Outline each Plasmodium ovale-infected red blood cell.
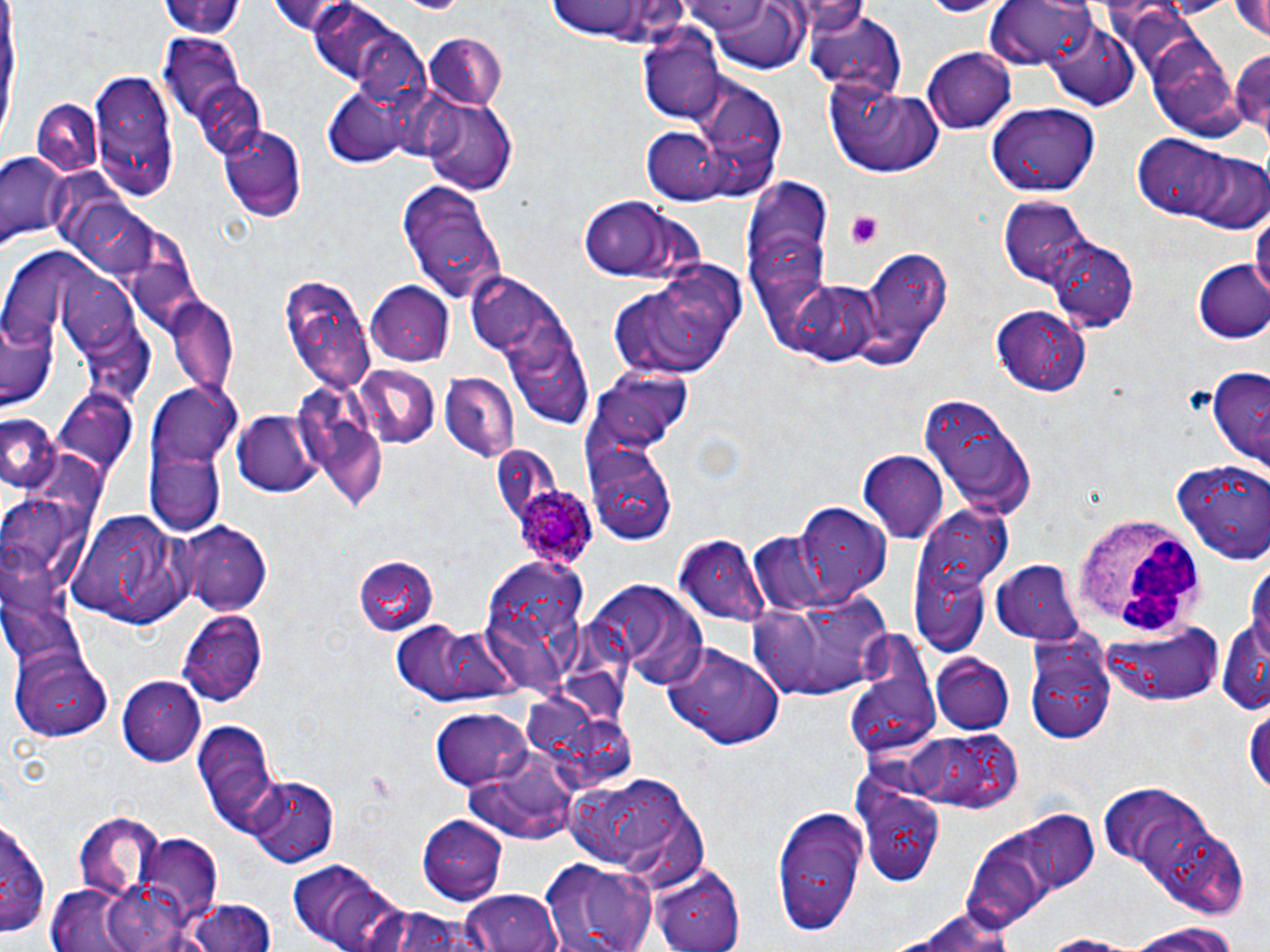

Approximate bounding boxes as (x1,y1)-(x2,y2) corner pairs in pixels.
Plasmodium ovale-infected red blood cells: (515,485)-(602,571).

White blood cell locations: (1070,515)-(1203,641). Platelet locations: (845,210)-(887,249), (364,771)-(395,799). Uninfected red blood cell locations: (154,0)-(246,42), (267,0)-(367,37), (542,0)-(693,47), (698,0)-(813,74), (985,0)-(1098,70), (1228,0)-(1270,44), (921,1)-(1000,17), (303,3)-(428,93), (800,7)-(908,98), (1046,24)-(1137,109), (638,29)-(726,124), (425,33)-(507,111), (1144,34)-(1244,139), (162,35)-(242,119), (923,47)-(1018,134), (1230,47)-(1270,138), (88,72)-(177,200), (194,76)-(267,167), (825,76)-(944,179), (674,77)-(789,200), (318,94)-(409,169), (422,97)-(516,194), (31,101)-(103,178), (986,103)-(1100,195), (218,123)-(309,223), (642,130)-(730,203), (1134,134)-(1236,220), (1178,148)-(1268,232), (2,153)-(69,250), (396,179)-(507,306), (742,181)-(835,319), (580,196)-(706,284), (999,198)-(1092,288), (74,201)-(161,281), (1252,206)-(1269,310), (1043,235)-(1139,332), (858,246)-(954,368), (1194,260)-(1270,344), (610,265)-(743,382), (59,268)-(141,357), (281,271)-(376,397), (472,271)-(546,358), (366,280)-(453,366), (788,280)-(883,367), (164,293)-(240,394), (991,305)-(1091,396), (4,311)-(58,412), (357,363)-(441,449), (1202,366)-(1270,474), (440,373)-(518,461), (51,385)-(139,484), (145,387)-(240,535), (919,396)-(1035,520), (233,409)-(320,497), (319,411)-(389,516), (0,412)-(59,496), (586,450)-(676,544), (859,452)-(950,543), (1171,457)-(1270,563), (0,497)-(72,576), (793,502)-(892,599), (68,507)-(197,626), (906,515)-(1005,659), (182,520)-(273,615), (749,534)-(840,613), (675,536)-(769,625), (0,544)-(55,622), (352,557)-(437,637), (991,559)-(1086,644), (476,560)-(592,699), (584,580)-(709,688), (1221,583)-(1270,717), (749,588)-(894,704), (177,609)-(266,705), (1101,619)-(1228,707), (388,621)-(514,707), (1024,629)-(1117,745), (844,631)-(939,756), (662,642)-(783,747), (11,645)-(115,743), (932,656)-(1014,734), (120,675)-(209,765), (525,698)-(604,770), (1243,699)-(1270,802), (430,708)-(531,791), (191,718)-(280,833), (903,732)-(1012,811), (562,773)-(704,875), (247,776)-(338,867), (851,778)-(948,887), (1096,779)-(1221,881), (770,805)-(871,931), (1009,809)-(1097,896), (74,811)-(164,893), (2,815)-(50,937), (419,816)-(507,904), (1138,821)-(1255,918), (135,837)-(225,928), (539,859)-(658,952), (286,860)-(412,952), (651,863)-(744,952), (44,882)-(156,952), (463,888)-(566,952), (181,898)-(278,951), (895,905)-(1024,952), (362,908)-(489,952), (1119,919)-(1245,951), (1028,931)-(1153,951). Slide-level diagnosis: Plasmodium ovale. Image is 1270×952 pixels. Thin blood film. Light microscopy. One field of a larger specimen. Captured at 1000x magnification. May-Grünwald-Giemsa-stained preparation.